Classify this cell by malaria status.
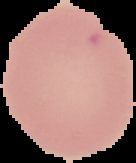

Uninfected.

From a thin blood smear. Image is 136×163 pixels. Cell region segmented out of the field of view; the surrounding area is masked to black.